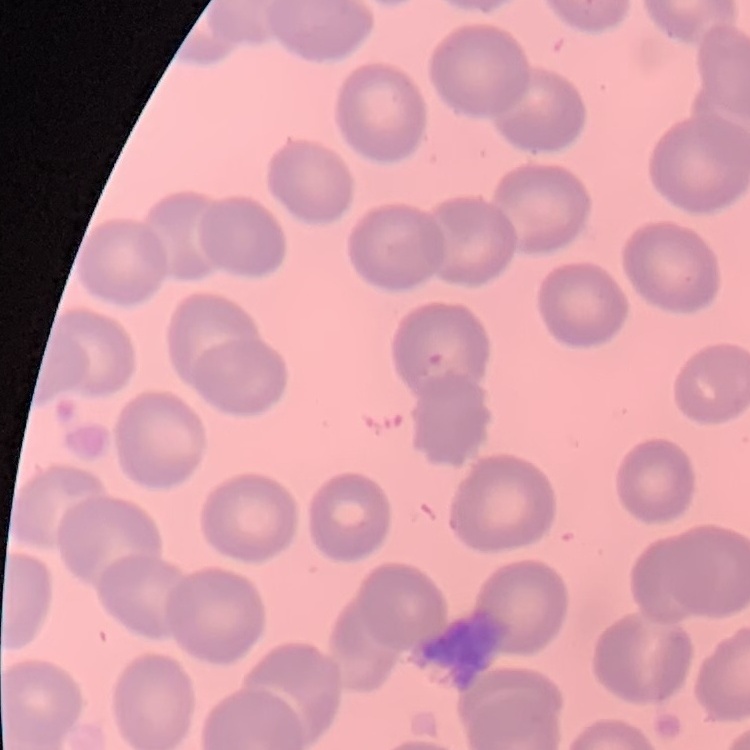

The red blood cells show no rouleaux formation. Stained with either Field's or Giemsa. Square crop of a larger photomicrograph. Thin blood smear.